Give the extent of all Plasmodium falciparum-infected red blood cells.
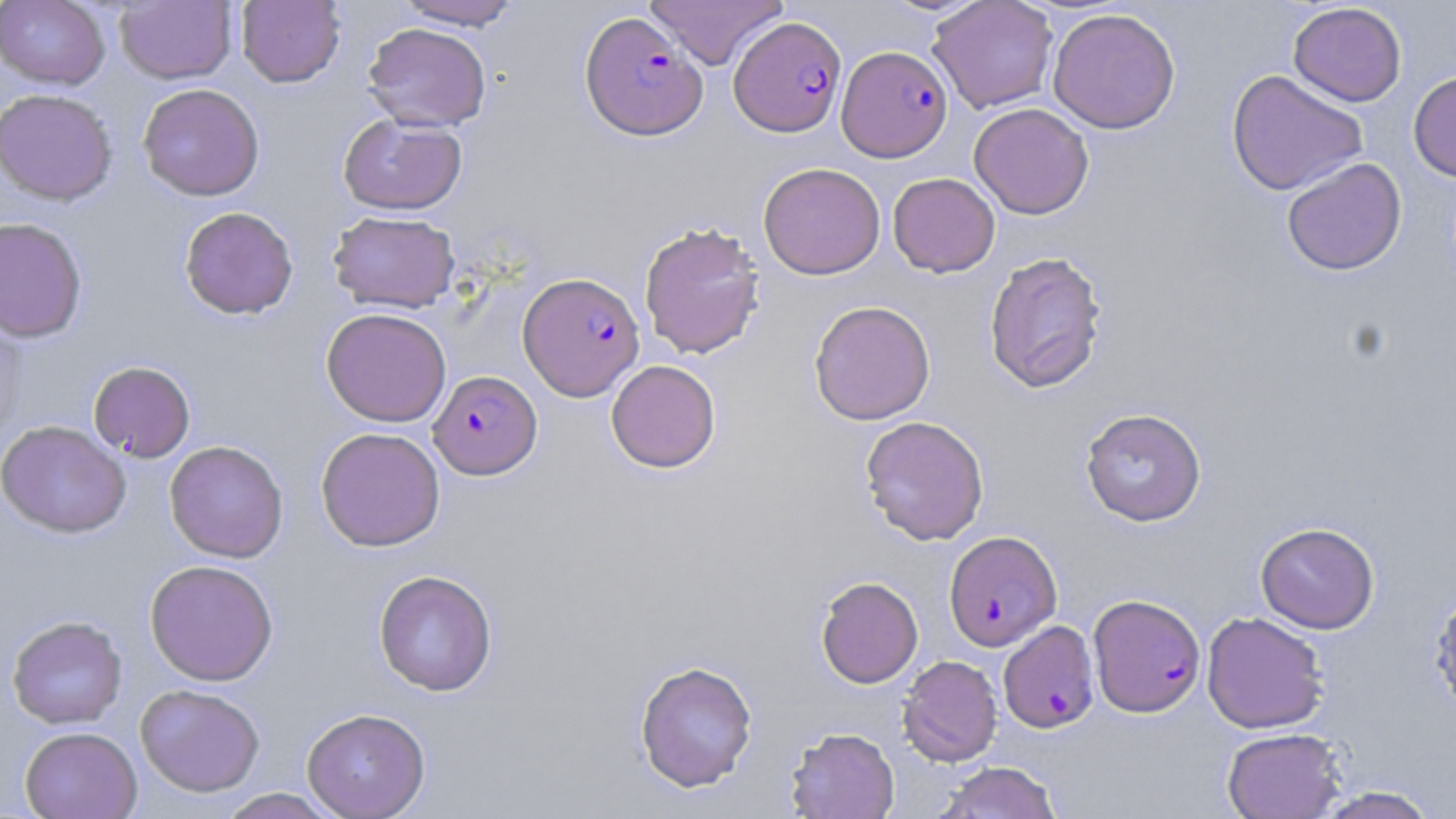
Approximate bounding boxes as (x1,y1)-(x2,y2) corner pairs in pixels.
Plasmodium falciparum-infected red blood cells: (580,10)-(708,141), (729,16)-(846,136), (837,45)-(952,162), (518,272)-(644,400), (429,371)-(542,479), (944,531)-(1062,650), (1089,593)-(1205,717), (998,620)-(1099,732).

Uninfected red blood cell locations: (0,0)-(110,89), (236,0)-(346,87), (390,0)-(524,29), (645,0)-(787,70), (927,0)-(1058,114), (115,1)-(237,84), (1288,2)-(1407,107), (1047,7)-(1181,135), (362,22)-(491,131), (1225,69)-(1367,196), (1408,71)-(1456,183), (137,83)-(265,201), (0,88)-(118,206), (969,102)-(1094,219), (338,113)-(467,215), (1281,157)-(1406,276), (758,162)-(885,280), (888,173)-(1000,277), (179,206)-(299,320), (328,210)-(460,313), (0,217)-(87,343), (638,221)-(765,360), (984,250)-(1108,394), (809,300)-(935,425), (321,307)-(451,427), (0,310)-(27,443), (606,359)-(721,473), (88,361)-(196,462), (1080,407)-(1206,526), (859,415)-(990,545), (0,420)-(132,538), (315,427)-(446,552), (164,440)-(288,562), (1256,522)-(1379,633), (144,559)-(279,686), (373,569)-(498,696), (816,576)-(923,688), (1429,584)-(1456,720), (1201,611)-(1330,733), (7,615)-(127,729), (898,655)-(1002,767), (634,660)-(758,793), (135,683)-(265,797), (301,707)-(430,819), (19,727)-(142,819), (785,727)-(900,819), (1221,727)-(1346,819), (935,762)-(1062,819), (1311,785)-(1442,818), (217,789)-(340,818). Slide-level diagnosis: Plasmodium falciparum. Light microscopy. 1000x magnification. Image is 1456×819 pixels. May-Grünwald-Giemsa stain. One field of a larger specimen. Thin blood smear.